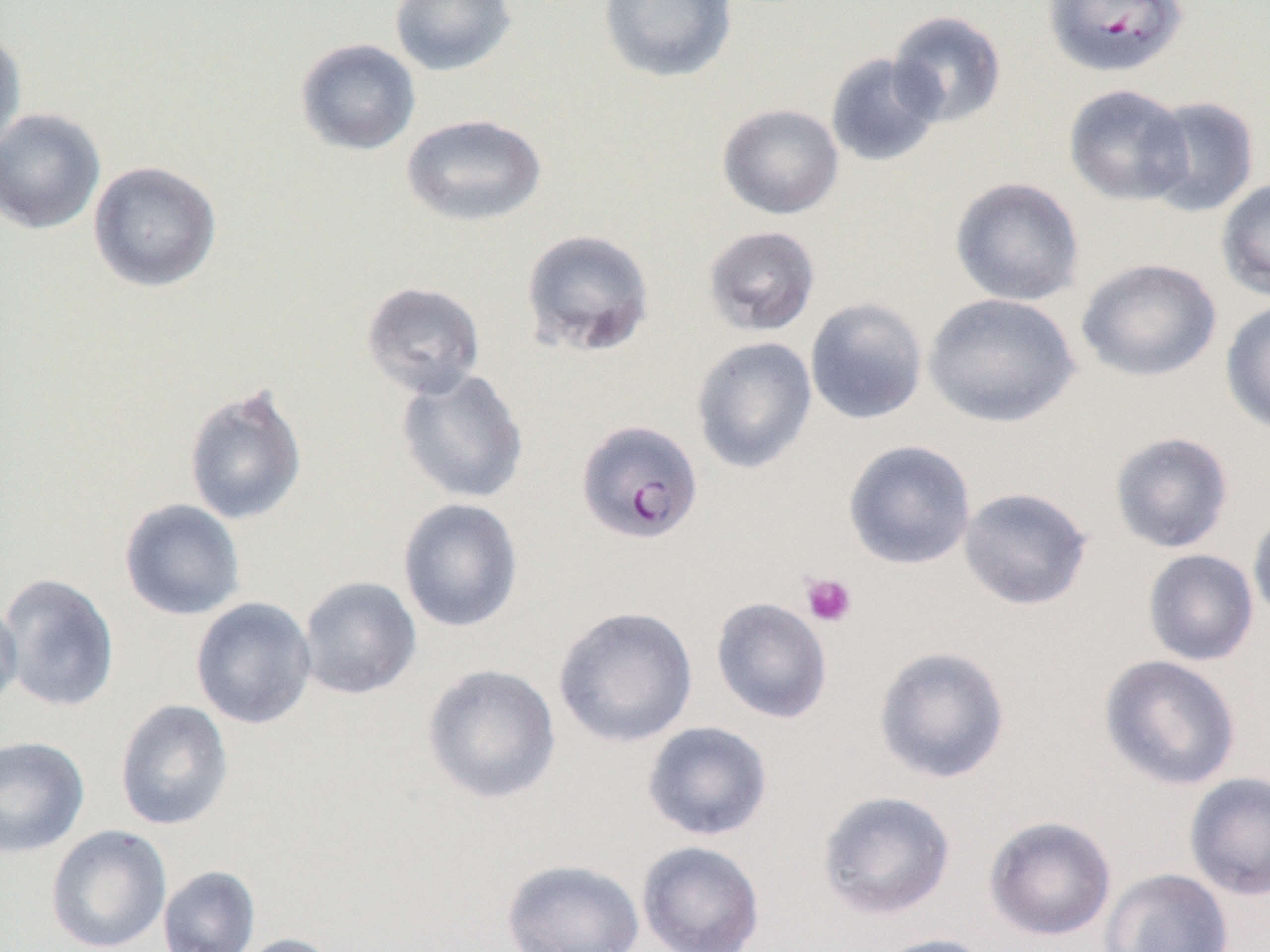
Summary:
  - Coordinate format: approximate bounding boxes as (x1, y1, x2, y2) in pixels
  - Platelet locations: (800, 572, 857, 628)
  - Uninfected red blood cell locations: (389, 0, 517, 76), (598, 0, 738, 84), (887, 10, 1007, 128), (0, 27, 27, 156), (295, 38, 421, 156), (825, 53, 943, 168), (1063, 84, 1193, 206), (1142, 95, 1260, 217), (717, 103, 844, 220), (0, 107, 106, 235), (401, 113, 547, 227), (88, 160, 222, 292), (949, 176, 1085, 306), (1216, 177, 1270, 302), (702, 225, 821, 337), (520, 228, 655, 357), (1076, 257, 1222, 382), (361, 281, 485, 399), (923, 292, 1081, 428), (804, 297, 928, 425), (1220, 299, 1270, 436), (691, 336, 817, 474), (395, 368, 529, 505), (183, 382, 308, 526), (1109, 431, 1235, 554), (842, 439, 976, 570), (957, 486, 1094, 611), (397, 497, 524, 633), (119, 498, 246, 621), (1248, 508, 1270, 626), (1142, 549, 1259, 667), (0, 572, 121, 713), (298, 576, 422, 699), (0, 595, 23, 714), (710, 596, 833, 724), (190, 597, 317, 729), (552, 605, 699, 747), (873, 644, 1011, 784), (1098, 654, 1243, 791), (421, 663, 561, 804), (114, 699, 234, 831), (641, 721, 773, 841), (0, 736, 90, 858), (1184, 771, 1270, 900), (816, 789, 956, 921), (983, 815, 1117, 940), (45, 824, 172, 952), (637, 840, 766, 952), (501, 858, 645, 952), (157, 864, 261, 952), (1100, 868, 1235, 952), (232, 933, 344, 952), (870, 933, 999, 952)
  - Plasmodium falciparum-infected red blood cell locations: (1042, 0, 1189, 79), (575, 419, 704, 544)
  - Slide-level diagnosis: Plasmodium falciparum
  - Magnification: 1000x
  - Image size: 1270×952 pixels
  - Preparation: thin blood film
  - Field of view: one of a larger specimen
  - Modality: light microscopy